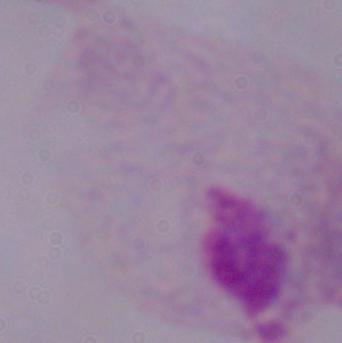 Micrograph. 1000x magnification. A trichomonad is shown.